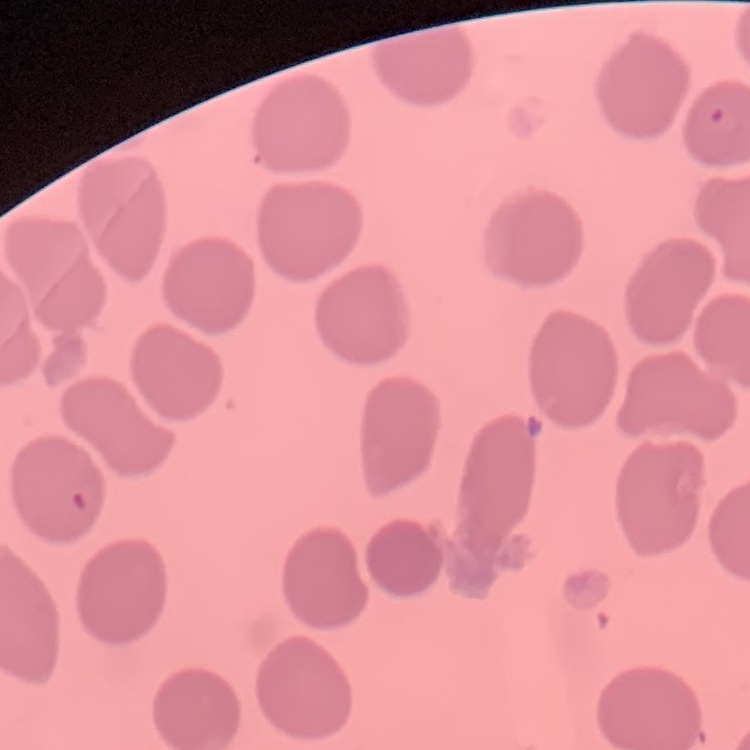

red_blood_cell_morphology: no rouleaux formation
stain: Field's or Giemsa
image_type: one tile cut from a larger photomicrograph
preparation: thin peripheral smear